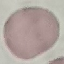
Result: no malaria parasites seen. Cell patch, automatically extracted from a larger field of view and resized to 64 × 64 pixels. Acquired by smartphone through the microscope eyepiece. Giemsa-stained preparation. Thin blood smear.